Point out each malaria parasite.
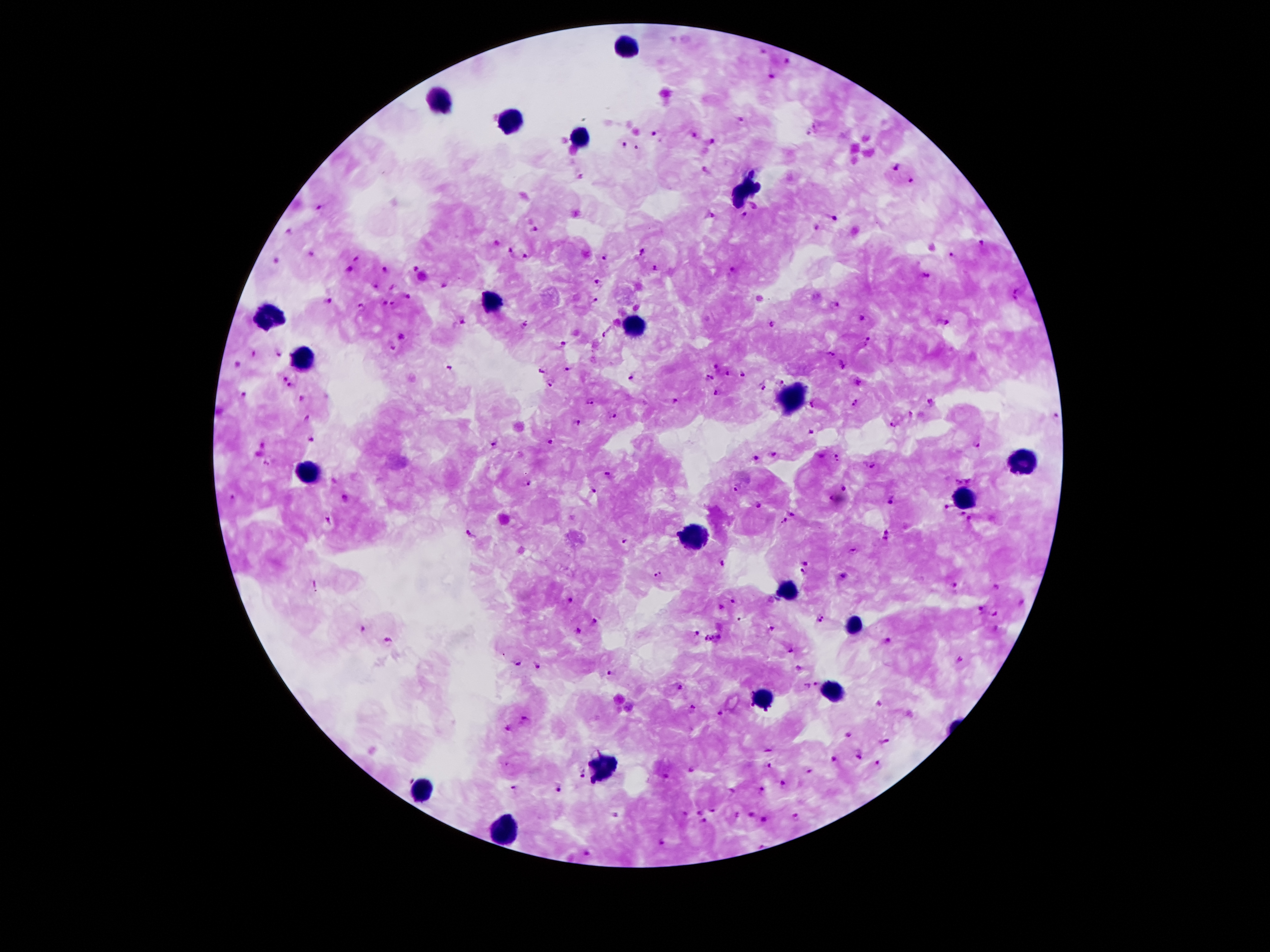
Approximate centers as [x, y] in pixels.
Malaria parasites: [761, 52], [789, 62], [773, 78], [740, 120], [655, 134], [691, 134], [712, 141], [624, 144], [896, 169], [911, 180], [319, 206], [744, 215], [711, 216], [834, 220], [535, 229], [816, 229], [288, 231], [980, 245], [511, 250], [643, 250], [312, 253], [951, 255], [523, 257], [605, 258], [277, 259], [358, 259], [416, 267], [385, 269], [655, 269], [349, 270], [733, 270], [927, 274], [597, 281], [444, 286], [376, 287], [1016, 294], [408, 297], [595, 299], [327, 302], [837, 303], [359, 304], [384, 304], [395, 304], [864, 318], [462, 322], [524, 323], [948, 324], [772, 325], [607, 333], [401, 337], [869, 340], [563, 343], [393, 348], [253, 353], [277, 353], [831, 355], [842, 364], [237, 366], [451, 366], [715, 366], [570, 369], [543, 370], [728, 372], [742, 373], [283, 377], [633, 377], [710, 378], [860, 380], [783, 384], [551, 385], [763, 385], [292, 387], [716, 392], [243, 394], [303, 399], [677, 399], [856, 401], [591, 402], [932, 402], [814, 403], [613, 416], [1053, 417], [309, 418], [577, 422], [895, 424], [810, 430], [311, 441], [493, 442], [549, 443], [263, 444], [978, 445], [774, 455], [837, 458], [755, 459], [269, 462], [872, 466], [609, 476], [959, 481], [971, 481], [526, 484], [843, 488], [736, 489], [593, 492], [232, 499], [830, 499], [891, 502], [759, 506], [945, 508], [795, 514], [963, 514], [783, 519], [969, 520], [329, 521], [471, 534], [886, 536], [623, 542], [853, 552], [805, 562], [721, 565], [803, 572], [657, 574], [843, 577], [956, 586], [996, 588], [571, 599], [733, 601], [1022, 603], [980, 608], [994, 614], [819, 617], [595, 623], [770, 628], [362, 629], [578, 631], [696, 633], [715, 640], [887, 642], [389, 643], [790, 651], [518, 662], [960, 662], [540, 666], [800, 668], [612, 673], [816, 683], [807, 686], [677, 688], [880, 704], [692, 710], [720, 714], [526, 719], [509, 729], [848, 736], [885, 741], [770, 749], [858, 754], [832, 758], [878, 763], [770, 767], [691, 770], [583, 773], [811, 773], [666, 778], [785, 787], [514, 788], [559, 789], [731, 791], [763, 791], [713, 811], [698, 812], [686, 813], [751, 814], [616, 815], [737, 815], [795, 817], [704, 820], [762, 820], [660, 841], [585, 852].

{
  "field_of_view": "one from this slide",
  "patient_malaria_status": "infected with Plasmodium falciparum",
  "image_size": "1270×952 pixels",
  "capture": "smartphone camera through the microscope eyepiece",
  "leukocyte_locations": "approximate centers as [x, y] in pixels: [628, 48], [438, 102], [509, 122], [580, 140], [744, 194], [491, 302], [270, 317], [633, 327], [299, 361], [790, 399], [1017, 463], [310, 479], [962, 499], [697, 541], [786, 591], [854, 625], [834, 692], [765, 700], [606, 764], [425, 787], [507, 826]",
  "magnification": "100x",
  "preparation": "thick peripheral-blood smear",
  "stain": "Giemsa"
}